Locate every uninfected red blood cell.
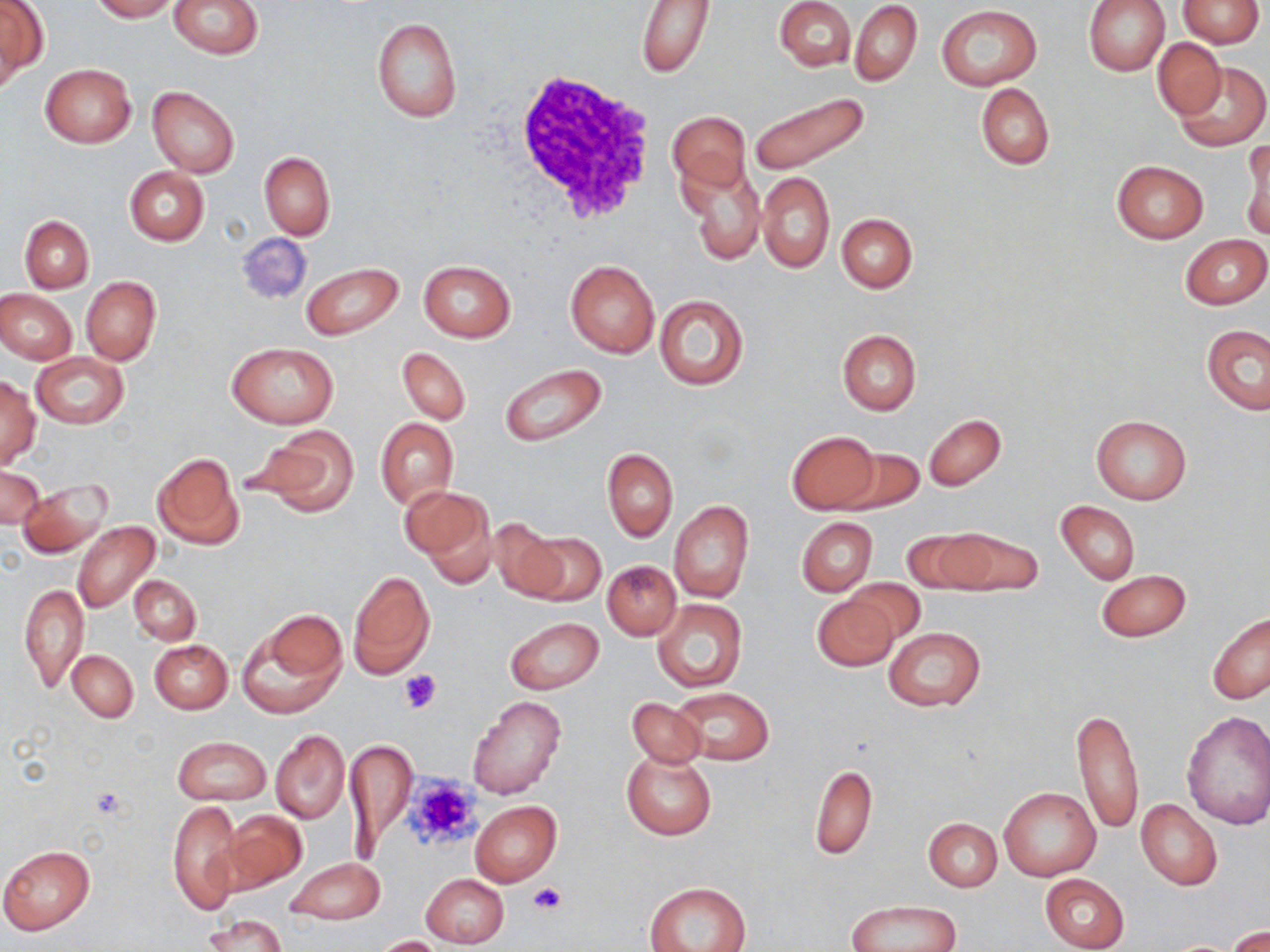
Approximate bounding boxes as [x1, y1, x2, y2] in pixels.
Uninfected red blood cells: [0, 0, 47, 83], [90, 0, 176, 21], [169, 0, 262, 58], [774, 0, 854, 71], [1083, 0, 1170, 76], [1178, 0, 1264, 47], [637, 1, 714, 77], [850, 1, 922, 86], [935, 5, 1042, 89], [370, 15, 462, 124], [1152, 37, 1227, 120], [1172, 59, 1268, 152], [40, 64, 136, 147], [975, 83, 1054, 170], [148, 85, 240, 178], [749, 92, 870, 178], [669, 108, 750, 193], [1242, 137, 1270, 239], [258, 151, 335, 240], [680, 159, 765, 264], [1112, 160, 1208, 244], [124, 167, 209, 246], [758, 171, 834, 273], [837, 213, 918, 292], [20, 215, 93, 294], [236, 231, 312, 306], [1180, 234, 1269, 309], [564, 259, 660, 358], [417, 260, 516, 342], [301, 262, 403, 341], [81, 276, 160, 366], [1, 289, 76, 363], [654, 294, 749, 392], [1201, 324, 1270, 415], [836, 329, 922, 415], [225, 342, 339, 429], [398, 347, 470, 424], [31, 353, 128, 429], [500, 362, 608, 447], [0, 377, 40, 466], [923, 413, 1006, 490], [1090, 414, 1191, 504], [375, 418, 457, 510], [251, 427, 359, 516], [785, 430, 881, 514], [833, 445, 924, 515], [602, 448, 677, 542], [152, 452, 243, 549], [0, 466, 43, 530], [17, 479, 114, 559], [404, 487, 497, 585], [669, 500, 754, 602], [1056, 500, 1140, 583], [797, 517, 877, 596], [486, 519, 572, 603], [73, 522, 159, 614], [937, 526, 1044, 598], [901, 528, 993, 594], [523, 530, 604, 606], [603, 561, 680, 640], [1096, 568, 1191, 642], [349, 571, 435, 678], [130, 575, 200, 645], [842, 577, 928, 646], [19, 584, 88, 693], [812, 594, 900, 672], [652, 599, 747, 693], [239, 609, 347, 718], [1207, 612, 1269, 705], [504, 616, 603, 694], [883, 627, 986, 710], [149, 640, 232, 714], [68, 650, 138, 722], [671, 687, 775, 766], [466, 695, 567, 801], [626, 696, 707, 769], [1072, 706, 1145, 834], [1181, 710, 1270, 829], [271, 728, 349, 824], [173, 737, 270, 805], [345, 737, 416, 853], [622, 753, 716, 840], [809, 765, 877, 860], [1000, 787, 1099, 881], [167, 799, 244, 914], [1136, 799, 1222, 891], [470, 801, 562, 887], [222, 810, 306, 893], [924, 817, 1001, 892], [0, 845, 95, 934], [284, 856, 385, 925], [420, 873, 509, 948], [1039, 873, 1130, 951], [644, 883, 751, 952], [848, 901, 960, 952], [202, 915, 286, 951], [1227, 926, 1270, 952], [372, 935, 445, 951].

Summary:
  - Platelet locations: [398, 668, 441, 715], [402, 773, 486, 855], [527, 883, 566, 916]
  - White blood cell locations: [506, 72, 660, 225]
  - Slide-level diagnosis: no evidence of blood parasites
  - Modality: optical microscopy
  - Preparation: thin blood smear
  - Field of view: single
  - Magnification: 1000x
  - Image size: 1270×952 pixels
  - Stain: May-Grünwald-Giemsa